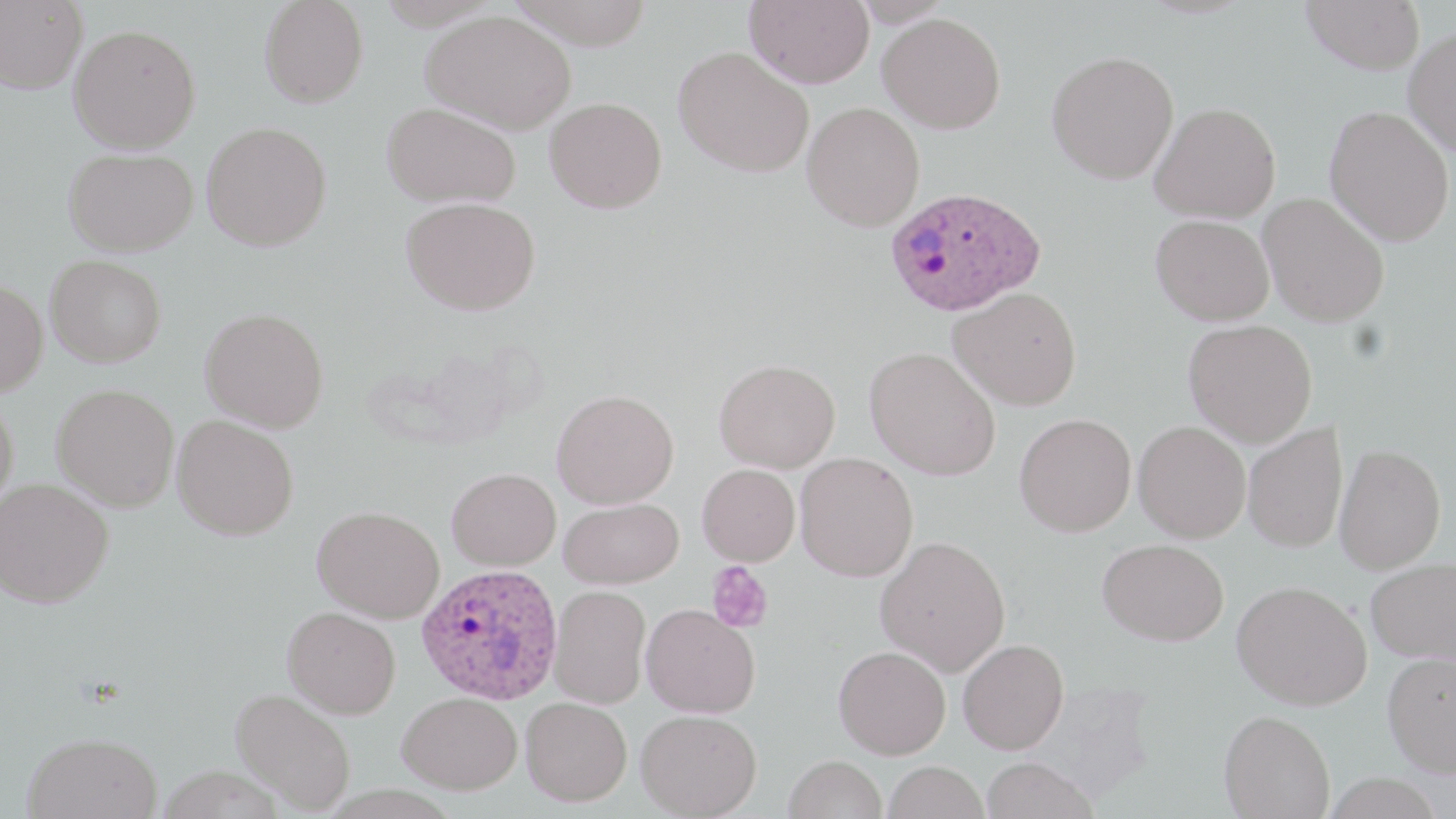
slide-level diagnosis = Plasmodium ovale
field of view = one of a larger specimen
image size = 1456×819 pixels
preparation = thin blood film
platelet locations = approximate bounding boxes as (x1, y1, x2, y2) in pixels: (706, 561, 774, 634)
modality = light microscopy
stain = May-Grünwald-Giemsa
Plasmodium ovale-infected red blood cell locations = approximate bounding boxes as (x1, y1, x2, y2) in pixels: (884, 185, 1046, 316), (417, 563, 563, 705)
magnification = 1000x
uninfected red blood cell locations = approximate bounding boxes as (x1, y1, x2, y2) in pixels: (1, 0, 87, 94), (508, 0, 655, 50), (744, 0, 874, 88), (1301, 0, 1425, 74), (259, 1, 368, 107), (421, 10, 576, 134), (878, 13, 1006, 134), (68, 24, 201, 153), (1403, 27, 1456, 156), (674, 46, 813, 177), (1047, 50, 1179, 184), (545, 97, 667, 213), (802, 101, 925, 231), (381, 102, 522, 208), (1149, 102, 1280, 223), (1324, 106, 1454, 246), (201, 121, 332, 251), (64, 147, 199, 257), (1257, 192, 1390, 327), (401, 197, 541, 316), (1150, 214, 1274, 326), (45, 254, 167, 367), (0, 280, 48, 396), (949, 287, 1081, 409), (200, 307, 329, 433), (1183, 319, 1317, 447), (863, 347, 1001, 480), (714, 359, 840, 473), (52, 382, 180, 512), (551, 389, 679, 509), (0, 396, 19, 516), (1014, 413, 1136, 537), (172, 415, 299, 540), (1133, 421, 1251, 543), (1242, 423, 1348, 554), (1335, 444, 1446, 574), (795, 453, 918, 582), (697, 464, 800, 566), (447, 467, 561, 571), (0, 478, 114, 608), (558, 497, 684, 589), (312, 505, 444, 623), (875, 535, 1010, 676), (1098, 538, 1228, 645), (1366, 557, 1456, 666), (1231, 580, 1372, 710), (549, 585, 651, 709), (640, 604, 760, 718), (282, 606, 401, 718), (958, 638, 1069, 754), (833, 646, 950, 759), (1382, 651, 1456, 777), (230, 687, 356, 814), (398, 692, 523, 794), (521, 697, 632, 807), (636, 709, 762, 818), (1219, 709, 1335, 819), (22, 732, 162, 819), (783, 755, 887, 819), (980, 757, 1097, 819), (884, 761, 989, 819)